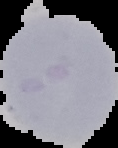

Malaria status: uninfected. Image is 118×148 pixels. From a thin blood smear. Cell region segmented out of the field of view; the surrounding area is masked to black.